State which parasite is depicted.
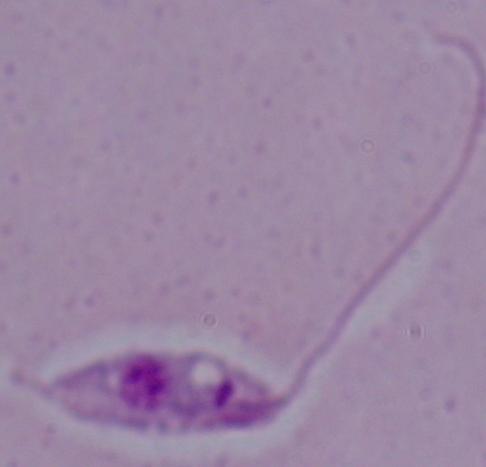

This is Leishmania.

Summary:
  - Magnification: 1000x
  - Modality: photomicrograph